Identify the blood parasite species.
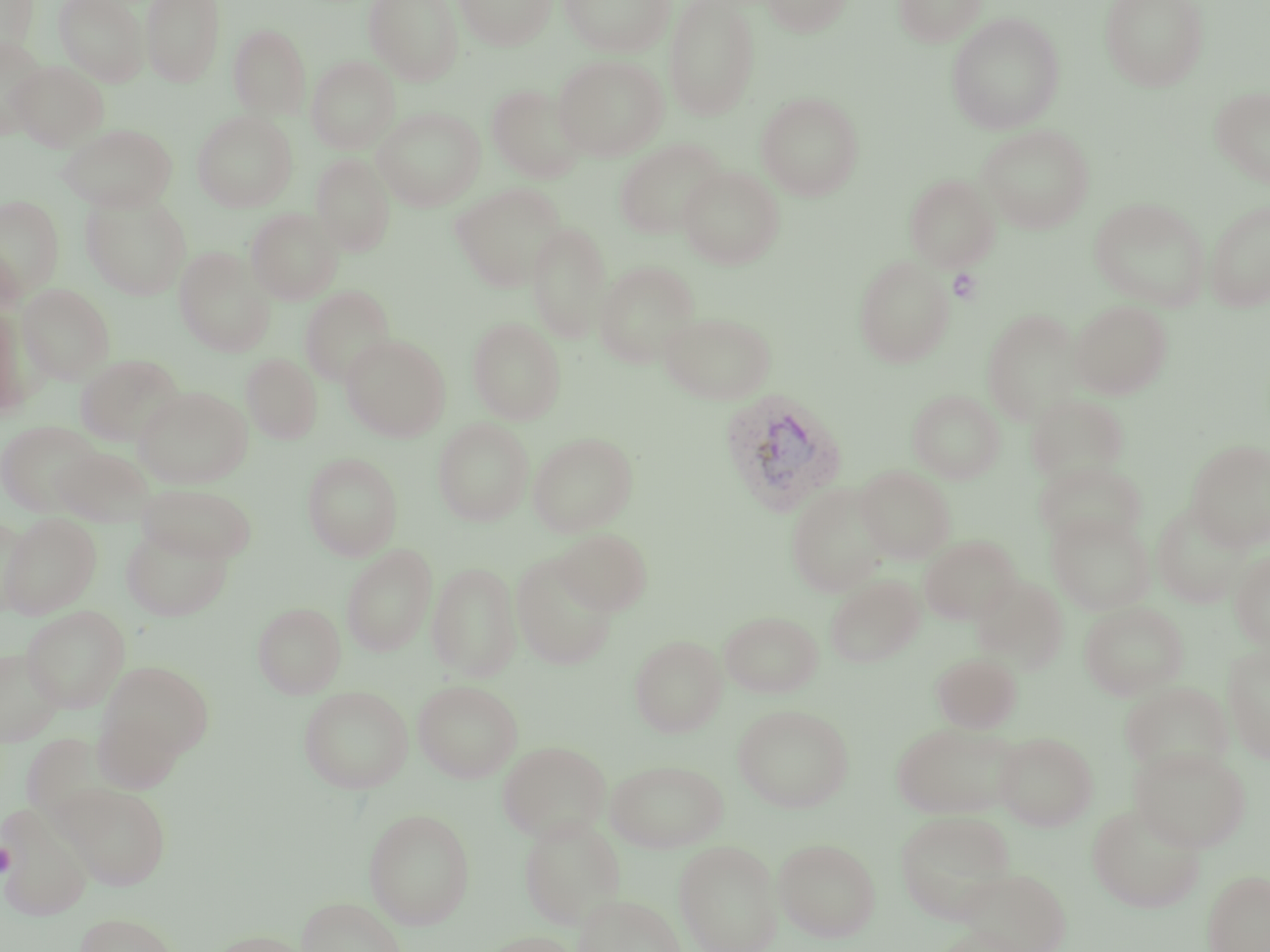

Plasmodium vivax.

Approximate bounding boxes as (x1, y1, x2, y2) in pixels. Plasmodium vivax-infected red blood cell locations: (718, 388, 847, 515). Platelet locations: (948, 268, 982, 304), (0, 842, 16, 877). Uninfected red blood cell locations: (53, 0, 149, 85), (141, 0, 226, 86), (364, 0, 463, 85), (455, 0, 556, 50), (559, 0, 675, 57), (663, 0, 761, 121), (760, 0, 852, 36), (894, 0, 988, 46), (1100, 0, 1209, 91), (0, 1, 38, 59), (946, 13, 1065, 134), (228, 23, 311, 119), (1, 35, 48, 137), (553, 54, 668, 161), (307, 55, 400, 154), (9, 60, 108, 151), (487, 84, 587, 183), (1210, 86, 1270, 188), (756, 92, 864, 201), (373, 108, 485, 210), (192, 110, 298, 212), (59, 123, 178, 212), (978, 125, 1094, 233), (614, 138, 725, 239), (311, 153, 396, 256), (678, 166, 784, 269), (904, 173, 1000, 271), (451, 183, 567, 291), (81, 192, 191, 299), (0, 195, 64, 297), (1088, 197, 1211, 311), (1205, 199, 1270, 311), (245, 207, 343, 305), (526, 222, 612, 343), (0, 242, 24, 320), (175, 247, 275, 356), (853, 255, 955, 368), (593, 260, 700, 367), (18, 284, 115, 384), (299, 285, 395, 386), (1070, 300, 1172, 399), (1, 303, 33, 418), (981, 308, 1085, 425), (658, 311, 776, 404), (467, 317, 566, 424), (341, 334, 450, 442), (241, 353, 322, 444), (75, 354, 185, 448), (134, 386, 252, 488), (907, 388, 1005, 483), (1026, 394, 1129, 485), (433, 418, 534, 526), (0, 420, 103, 516), (528, 432, 638, 537), (1187, 440, 1270, 550), (51, 446, 156, 525), (302, 451, 403, 560), (1034, 459, 1146, 550), (855, 465, 956, 563), (137, 483, 257, 564), (786, 483, 890, 597), (1153, 502, 1251, 607), (1047, 512, 1154, 614), (2, 513, 101, 618), (0, 515, 28, 618), (120, 524, 234, 622), (554, 528, 652, 616), (919, 535, 1020, 624), (341, 543, 437, 656), (1230, 550, 1270, 650), (512, 553, 619, 670), (427, 561, 521, 682), (970, 573, 1068, 673), (825, 575, 925, 668), (253, 601, 346, 698), (1080, 601, 1188, 700), (21, 605, 130, 712), (720, 610, 823, 698), (630, 635, 726, 737), (1222, 641, 1270, 764), (0, 649, 63, 744), (931, 652, 1022, 732), (97, 660, 215, 767), (413, 679, 523, 782), (1120, 681, 1234, 778), (299, 685, 413, 793), (733, 703, 854, 812), (92, 706, 187, 794), (890, 721, 1021, 819), (994, 731, 1098, 831), (499, 740, 611, 843), (1130, 745, 1250, 852), (606, 759, 728, 852), (59, 783, 171, 890), (1, 803, 93, 921), (1087, 803, 1206, 913), (363, 807, 475, 929), (895, 810, 1015, 921), (519, 816, 625, 930), (774, 837, 881, 942), (674, 839, 783, 952), (957, 868, 1071, 951), (1203, 869, 1270, 952), (574, 893, 687, 952), (297, 897, 407, 952), (73, 913, 180, 952), (932, 926, 1031, 952), (206, 930, 313, 952), (480, 931, 583, 952). Optical microscopy. May-Grünwald-Giemsa stain. One field of a larger specimen. Thin blood film. Captured at 1000x magnification. Image is 1270×952 pixels.